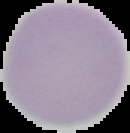 From a thin blood film. Cell region segmented out of the field of view; the surrounding area is masked to black. Malaria status: uninfected. Image is 130×133 pixels.